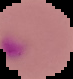 Image is 73×79 pixels. Result: malaria parasites identified. From a thin blood film. The area outside the segmented cell region is set to black.